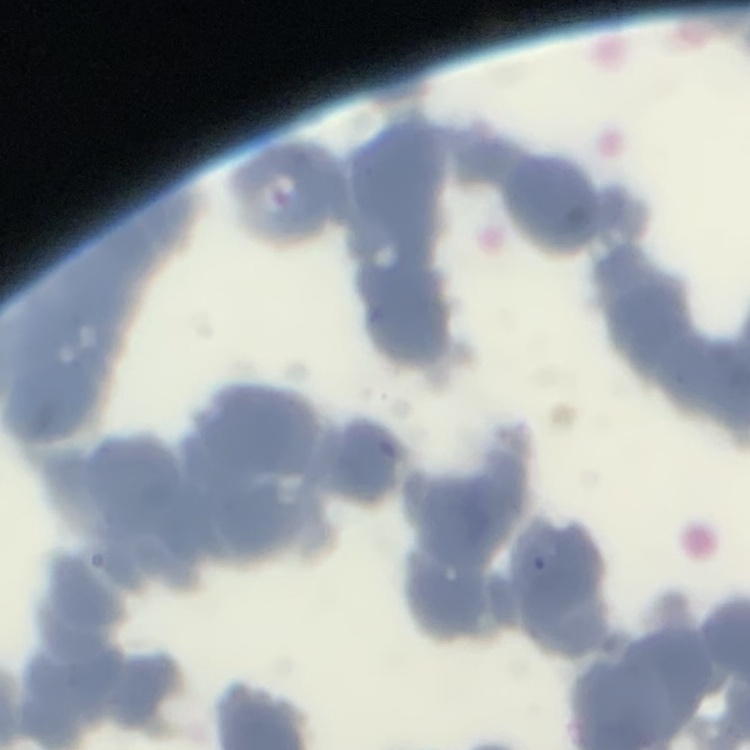 The red blood cells show rouleaux formation. One tile cut from a larger photomicrograph. Field's or Giemsa stain. Thin peripheral smear.